Identify the preparation type.
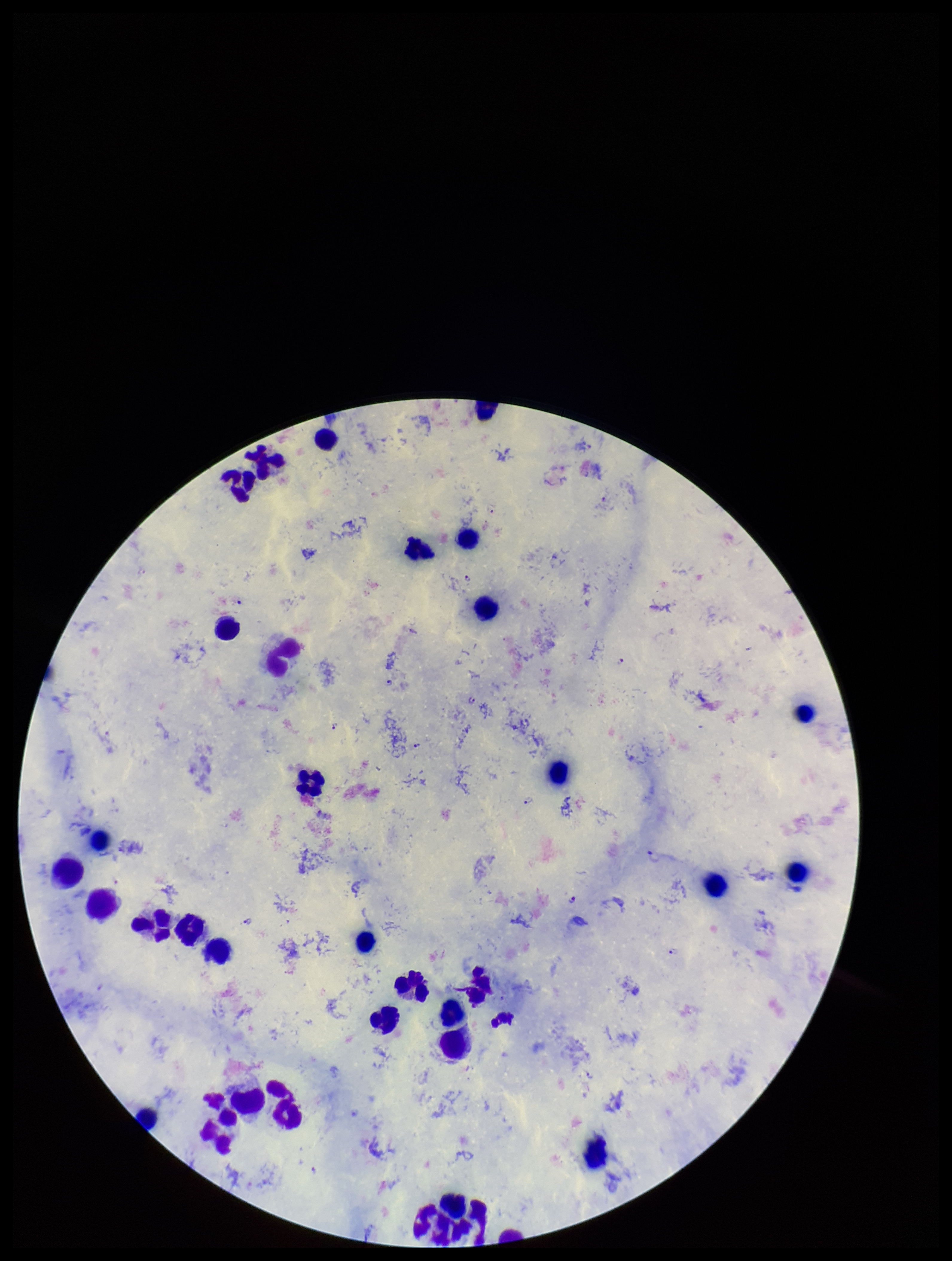
Thick.

stain = Giemsa
capture = smartphone photograph through the microscope eyepiece
Plasmodium parasites = identified
leukocyte count = 35
image size = 952×1261 pixels
patient malaria status = infected
species reported for this patient = Plasmodium falciparum
parasite count = 17
field of view = one from this slide